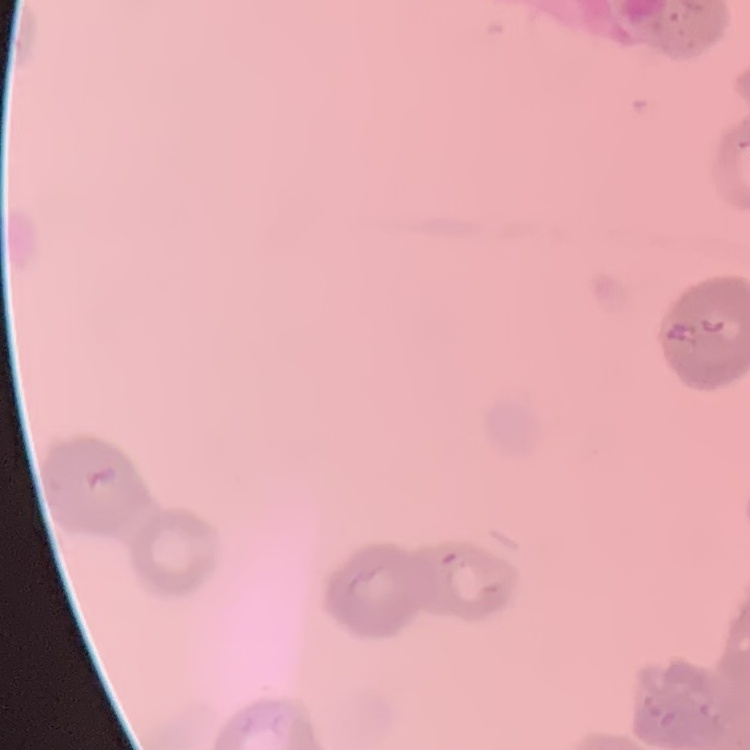
{
  "erythrocyte_morphology": "rouleaux formation",
  "image_type": "one tile cut from a larger photomicrograph",
  "preparation": "thin blood film",
  "stain": "Field's or Giemsa"
}